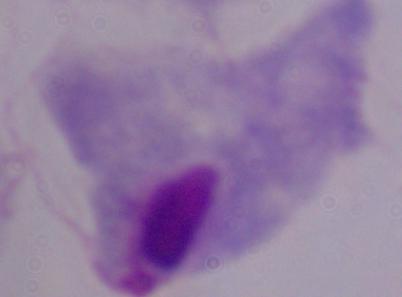

Summary:
  - Magnification: 1000x
  - Modality: micrograph
  - Identification: trichomonad